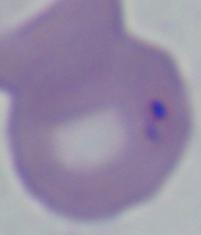

{
  "magnification": "1000x",
  "identification": "Babesia",
  "modality": "micrograph"
}